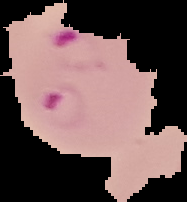

Summary:
  - Image size: 187×202 pixels
  - Image type: segmented cell region on a black background
  - Result: Plasmodium parasites identified
  - Preparation: thin blood film